Identify the blood parasite species.
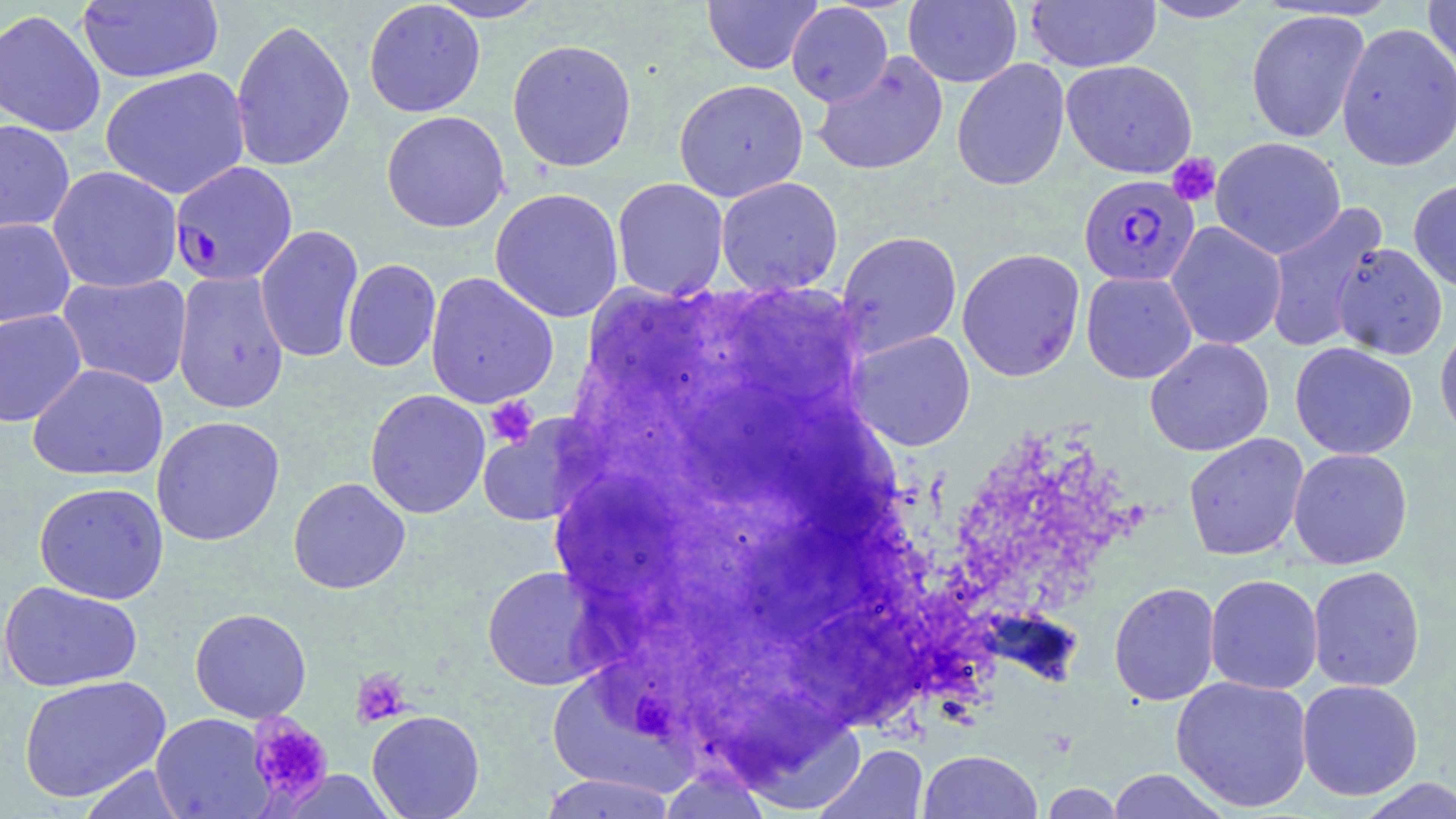
Plasmodium falciparum.

Summary:
  - Coordinate format: approximate bounding boxes as (x1,y1)-(x2,y2) corner pairs in pixels
  - Plasmodium falciparum-infected red blood cell locations: (169,161)-(298,286), (1078,174)-(1200,287)
  - Uninfected red blood cell locations: (427,0)-(551,23), (702,0)-(822,74), (903,0)-(1023,88), (1139,0)-(1263,23), (1422,0)-(1456,80), (77,1)-(223,84), (363,1)-(486,118), (1025,1)-(1161,72), (786,3)-(894,107), (0,8)-(106,138), (1245,9)-(1370,144), (231,18)-(355,173), (1336,23)-(1456,172), (506,38)-(638,173), (811,51)-(949,177), (951,58)-(1070,191), (1061,59)-(1198,179), (100,66)-(250,200), (673,78)-(809,202), (381,110)-(510,233), (0,119)-(75,237), (1210,137)-(1346,260), (47,165)-(183,293), (715,176)-(844,295), (611,178)-(729,300), (1408,178)-(1456,292), (489,187)-(624,323), (1263,203)-(1387,354), (0,218)-(76,327), (1166,221)-(1287,350), (254,225)-(364,363), (836,230)-(963,356), (1331,242)-(1448,360), (956,248)-(1086,382), (342,259)-(441,373), (172,271)-(290,414), (1081,271)-(1197,384), (56,273)-(193,390), (424,273)-(558,408), (0,308)-(87,427), (1435,321)-(1456,447), (848,330)-(975,450), (1144,337)-(1274,456), (1290,342)-(1418,460), (27,364)-(168,482), (365,389)-(490,519), (151,415)-(285,546), (1183,432)-(1309,561), (1288,448)-(1413,569), (288,477)-(411,594), (33,481)-(169,604), (481,565)-(603,691), (1307,565)-(1425,692), (1205,574)-(1323,695), (0,580)-(143,693), (1108,582)-(1221,706), (189,608)-(312,723), (18,675)-(171,803), (1171,675)-(1313,812), (1296,679)-(1423,800), (366,709)-(485,819), (150,713)-(274,818), (816,744)-(929,819), (918,750)-(1043,819), (76,764)-(192,818), (1105,769)-(1232,818), (537,773)-(680,818), (1353,778)-(1456,818)
  - Platelet locations: (1167,153)-(1221,207), (484,396)-(538,448), (351,668)-(411,727), (247,714)-(333,809)
  - Modality: light microscopy
  - Image size: 1456×819 pixels
  - Magnification: 1000x
  - Preparation: thin blood film
  - Stain: May-Grünwald-Giemsa
  - Field of view: single